Give the position of every Plasmodium parasite visible.
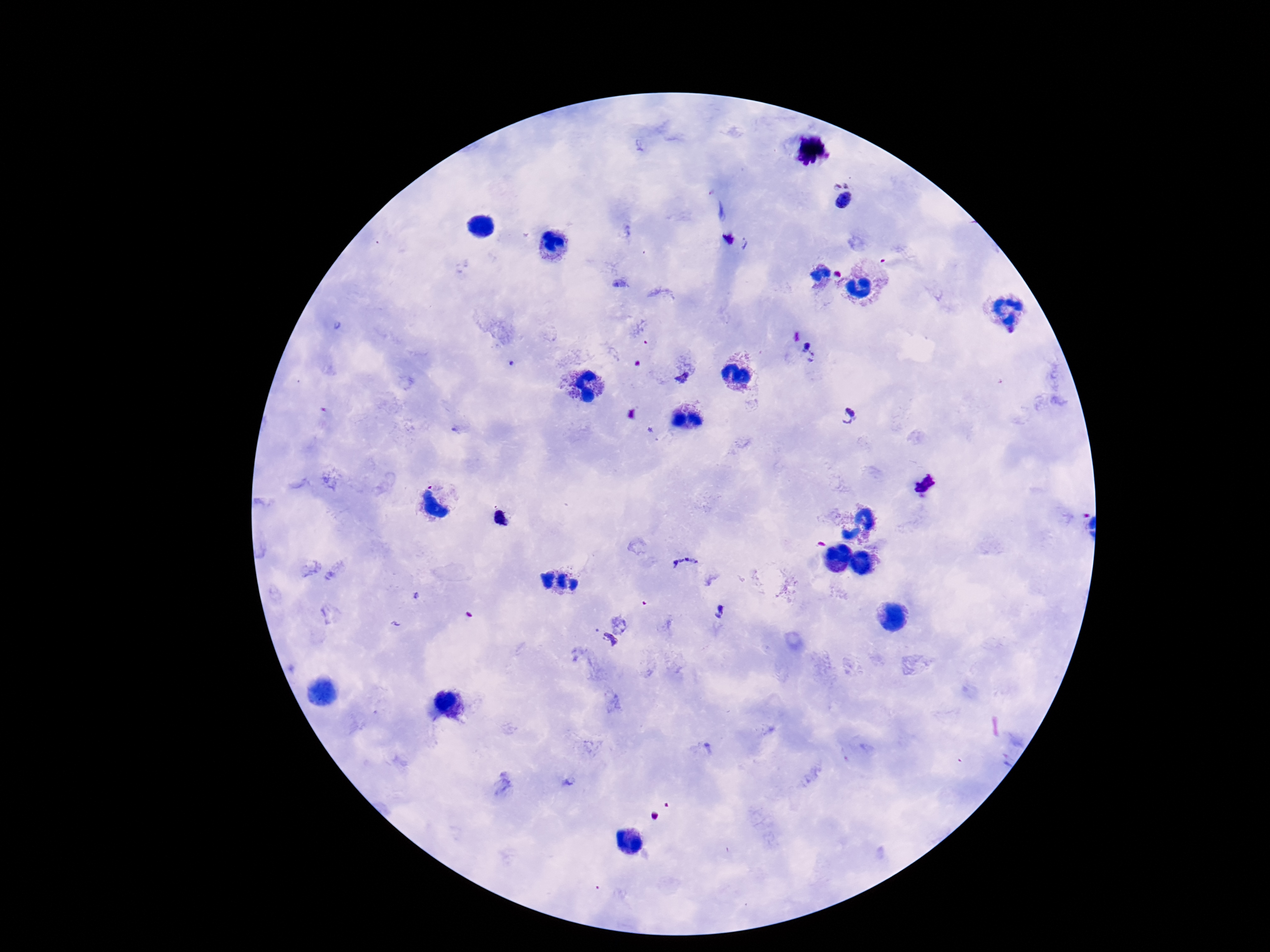
Approximate centers as {x, y} in pixels.
Plasmodium parasites: {843, 198}, {731, 240}, {808, 353}, {681, 377}, {851, 414}, {925, 483}, {502, 519}, {685, 567}, {718, 611}, {606, 643}.

One field from this slide. Image is 1270×952 pixels. Smartphone photograph taken through the microscope eyepiece. Thick blood smear. Giemsa stain. Patient malaria status: infected. 100x magnification.